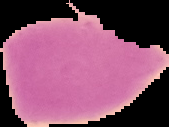
Malaria status: uninfected. From a thin blood smear. The area outside the segmented cell region is set to black. Image is 169×127 pixels.